Name the blood parasite species.
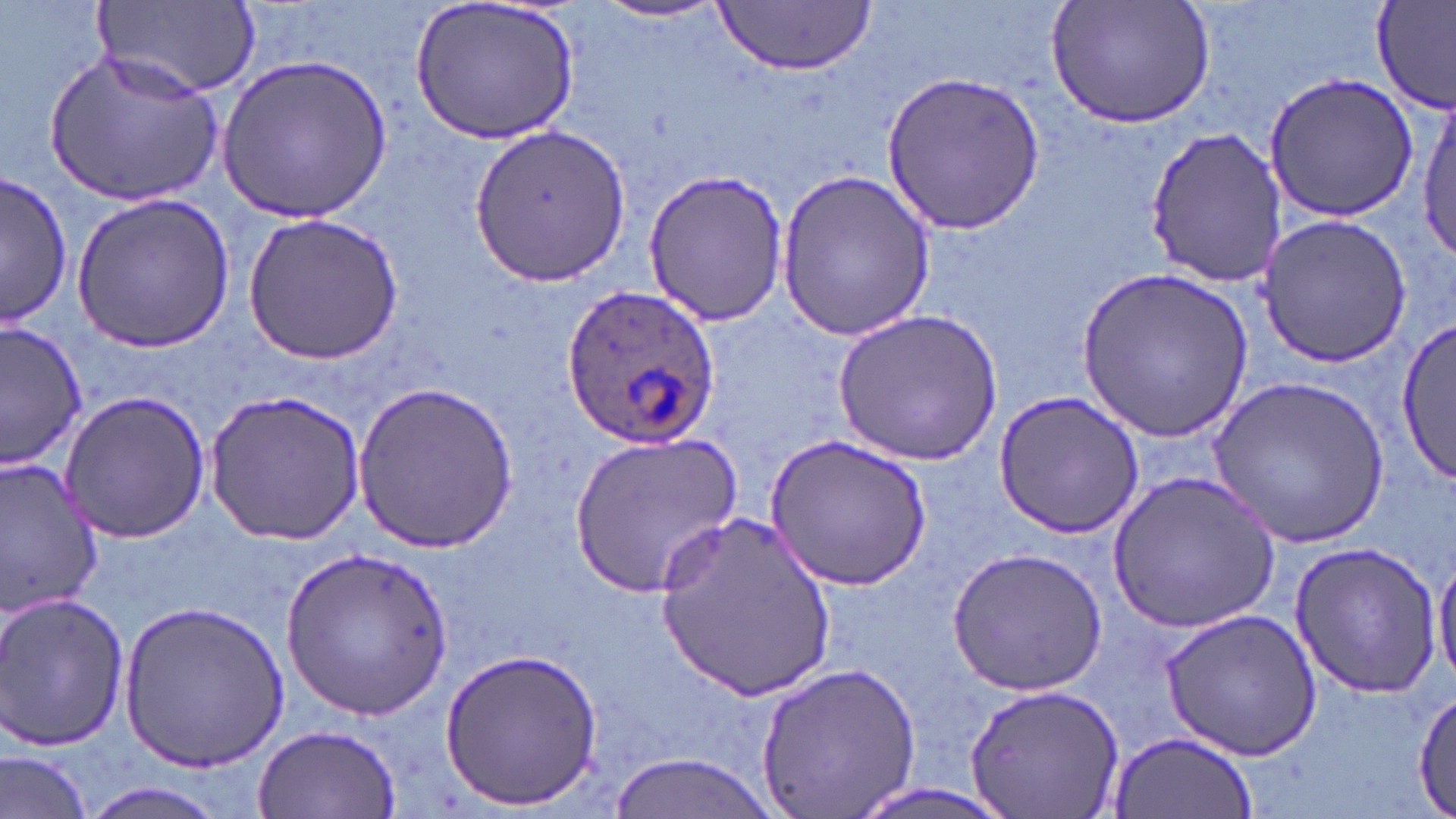

Plasmodium ovale.

uninfected red blood cell locations = approximate bounding boxes as named x1/y1/x2/y2 corners in pixels: (x1=91, y1=0, x2=260, y2=103), (x1=406, y1=0, x2=580, y2=147), (x1=1049, y1=0, x2=1216, y2=130), (x1=590, y1=1, x2=735, y2=25), (x1=714, y1=1, x2=877, y2=74), (x1=1372, y1=2, x2=1455, y2=114), (x1=44, y1=49, x2=224, y2=207), (x1=218, y1=54, x2=393, y2=224), (x1=884, y1=70, x2=1046, y2=234), (x1=1261, y1=71, x2=1423, y2=224), (x1=1417, y1=94, x2=1455, y2=270), (x1=469, y1=121, x2=631, y2=287), (x1=1143, y1=127, x2=1285, y2=286), (x1=776, y1=167, x2=936, y2=343), (x1=643, y1=168, x2=792, y2=327), (x1=1, y1=170, x2=72, y2=328), (x1=73, y1=193, x2=234, y2=352), (x1=241, y1=212, x2=408, y2=367), (x1=1255, y1=214, x2=1412, y2=367), (x1=1078, y1=265, x2=1252, y2=444), (x1=833, y1=308, x2=1002, y2=465), (x1=1, y1=320, x2=88, y2=471), (x1=1394, y1=322, x2=1456, y2=483), (x1=1211, y1=375, x2=1389, y2=548), (x1=353, y1=380, x2=517, y2=555), (x1=203, y1=389, x2=366, y2=548), (x1=61, y1=390, x2=212, y2=542), (x1=993, y1=390, x2=1144, y2=539), (x1=569, y1=434, x2=743, y2=594), (x1=769, y1=434, x2=933, y2=588), (x1=0, y1=457, x2=106, y2=612), (x1=1104, y1=470, x2=1281, y2=636), (x1=655, y1=513, x2=835, y2=700), (x1=1287, y1=540, x2=1442, y2=698), (x1=280, y1=546, x2=452, y2=718), (x1=948, y1=547, x2=1109, y2=695), (x1=1431, y1=549, x2=1456, y2=686), (x1=0, y1=592, x2=130, y2=750), (x1=120, y1=599, x2=289, y2=773), (x1=1159, y1=607, x2=1322, y2=761), (x1=438, y1=645, x2=605, y2=811), (x1=755, y1=660, x2=922, y2=819), (x1=963, y1=682, x2=1124, y2=819), (x1=1412, y1=686, x2=1454, y2=818), (x1=253, y1=725, x2=401, y2=816), (x1=1106, y1=728, x2=1258, y2=818), (x1=0, y1=747, x2=95, y2=819), (x1=606, y1=752, x2=782, y2=819), (x1=72, y1=780, x2=239, y2=818), (x1=835, y1=784, x2=1029, y2=819)
Plasmodium ovale-infected red blood cell locations = approximate bounding boxes as named x1/y1/x2/y2 corners in pixels: (x1=563, y1=283, x2=721, y2=449)
image size = 1456×819 pixels
stain = May-Grünwald-Giemsa
field of view = single
modality = optical microscopy
magnification = 1000x
preparation = thin blood film